Identify the blood parasite species.
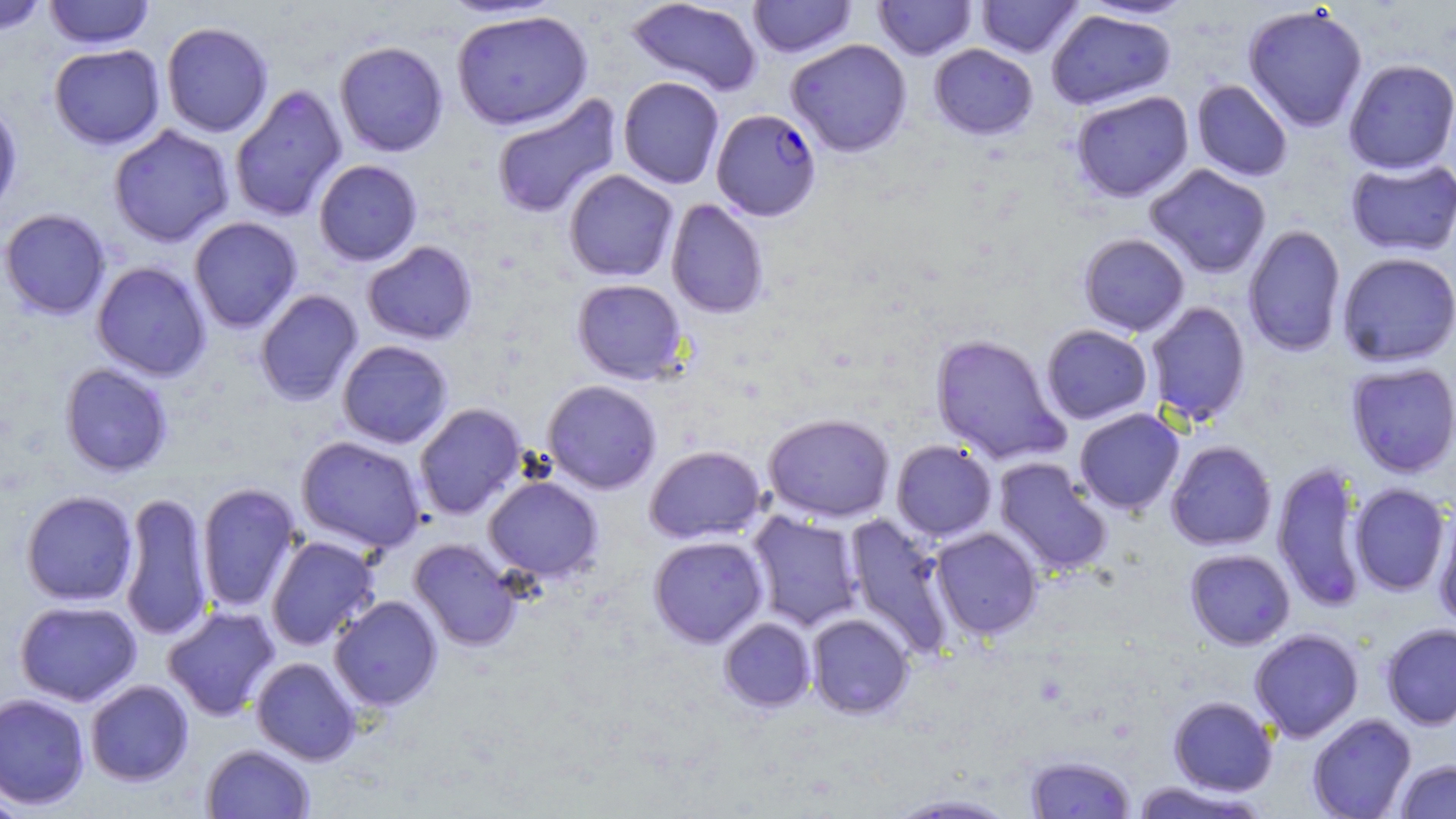
Plasmodium falciparum.

modality: optical microscopy
plasmodium_falciparum_infected_red_blood_cell_locations: 'approximate bounding boxes as (x1,y1)-(x2,y2) corner pairs in pixels: (711,108)-(822,221)'
magnification: 1000x
uninfected_red_blood_cell_locations: 'approximate bounding boxes as (x1,y1)-(x2,y2) corner pairs in pixels: (0,0)-(51,35), (43,0)-(155,49), (626,0)-(763,96), (747,0)-(857,58), (873,0)-(977,60), (976,0)-(1083,58), (1080,0)-(1195,20), (1243,4)-(1368,133), (1046,9)-(1175,111), (451,10)-(593,130), (161,21)-(273,138), (786,38)-(912,157), (334,40)-(449,157), (48,44)-(165,149), (928,44)-(1038,140), (1343,58)-(1456,174), (618,76)-(724,189), (1191,79)-(1293,182), (229,84)-(348,223), (1071,90)-(1194,202), (490,93)-(623,220), (0,98)-(23,220), (108,124)-(234,247), (1345,157)-(1456,256), (313,159)-(423,266), (1144,163)-(1271,278), (563,169)-(679,282), (666,198)-(769,319), (0,208)-(112,320), (188,216)-(303,333), (1243,224)-(1346,357), (1078,233)-(1190,336), (362,241)-(477,345), (1337,251)-(1456,367), (91,261)-(212,381), (572,278)-(688,384), (255,289)-(363,407), (1145,301)-(1251,426), (1040,324)-(1153,425), (930,333)-(1070,466), (337,340)-(454,449), (1346,362)-(1456,477), (59,363)-(173,477), (542,379)-(662,494), (414,402)-(528,520), (1074,408)-(1185,514), (763,413)-(895,522), (296,435)-(427,554), (891,440)-(997,542), (1165,440)-(1277,551), (645,445)-(766,544), (993,457)-(1112,577), (1272,460)-(1369,613), (484,475)-(603,581), (195,482)-(303,613), (1349,483)-(1451,596), (21,490)-(138,606), (119,491)-(213,643), (1433,508)-(1456,630), (746,510)-(864,632), (844,513)-(957,659), (930,527)-(1043,639), (265,535)-(380,651), (648,535)-(769,648), (408,538)-(522,652), (1185,548)-(1295,650), (329,595)-(443,711), (15,600)-(142,706), (162,605)-(281,721), (807,614)-(914,718), (719,617)-(816,711), (1380,623)-(1456,730), (1249,628)-(1364,742), (251,657)-(361,765), (85,679)-(194,786), (0,692)-(91,810), (1168,695)-(1277,796), (1307,713)-(1416,819), (201,743)-(315,818), (1025,754)-(1136,818), (1394,759)-(1456,818), (1129,780)-(1269,819), (0,792)-(30,818), (885,792)-(1022,817)'
stain: May-Grünwald-Giemsa
preparation: thin blood film
image_size: 1456×819 pixels
field_of_view: one of a larger specimen